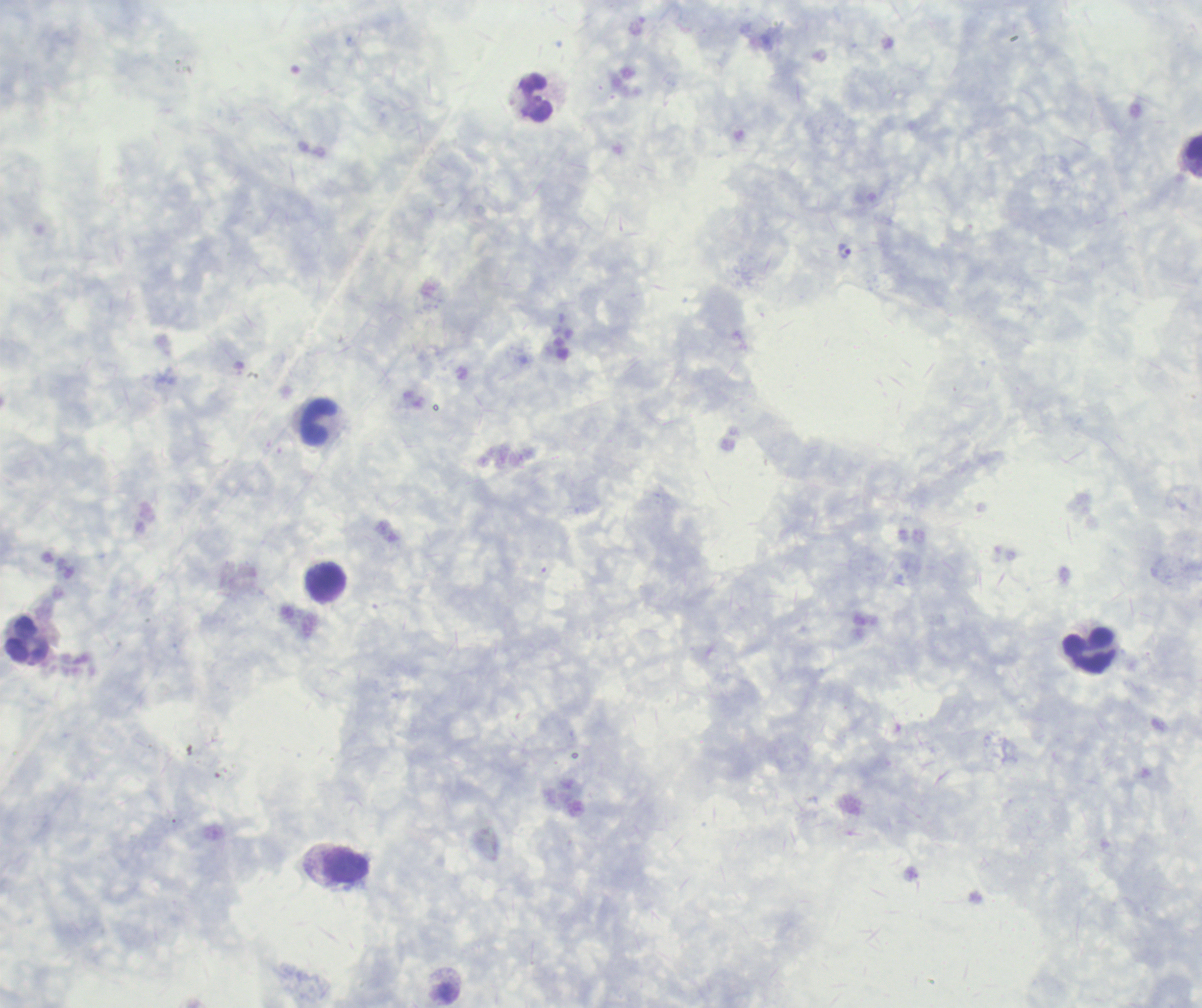

coordinate format = approximate centers as (x, y) in pixels
trophozoite locations = (845, 252)
leukocyte locations = (536, 99), (1194, 155), (319, 423), (325, 583), (27, 640), (1089, 651), (347, 866)
preparation = thick blood film
magnification = 100x
field of view = single
result = malaria parasites identified
coloration quality = good
context = previously used in an actual diagnosis
image size = 1202×1008 pixels
stain = Romanowsky
background quality = unsatisfactory